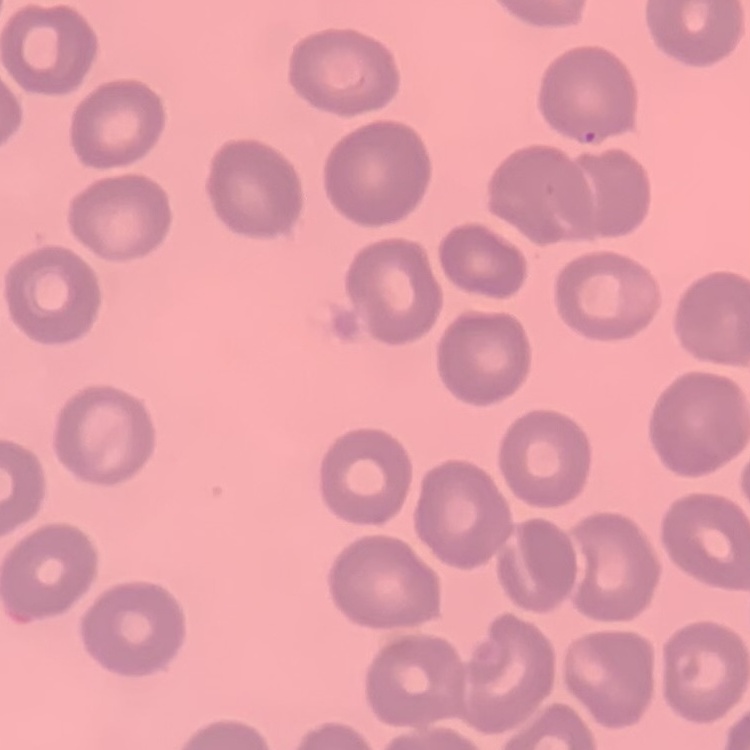

{
  "red_blood_cell_morphology": "no rouleaux formation",
  "stain": "Field's or Giemsa",
  "preparation": "thin peripheral smear",
  "image_type": "square crop of a larger photomicrograph"
}